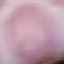 Result: no malaria parasites seen. Giemsa-stained preparation. Automatically extracted cell patch, resized to 64 × 64 pixels. Thin smear of blood. Photographed with a smartphone camera at the microscope eyepiece.